Assess this cell for malaria.
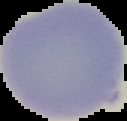
Uninfected.

Summary:
  - Image size: 127×121 pixels
  - Image type: segmented cell region with the area outside set to black
  - Preparation: thin blood film